Give the position of every leukocyte visible.
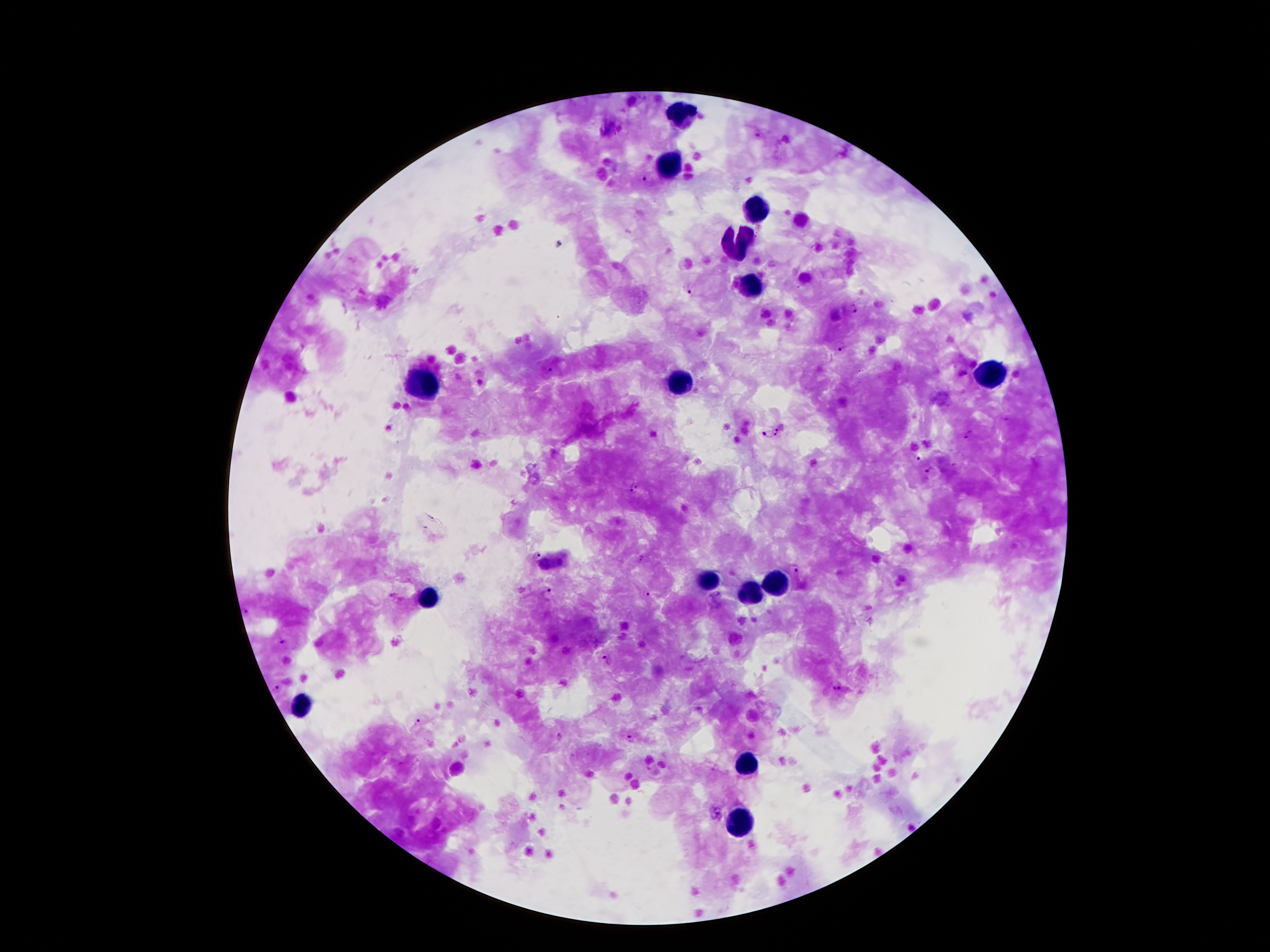

Approximate centers as [x, y] in pixels.
Leukocytes: [676, 115], [672, 163], [756, 207], [737, 241], [750, 287], [989, 375], [422, 383], [678, 385], [708, 581], [777, 581], [752, 593], [428, 598], [302, 707], [746, 763], [739, 822].

Malaria parasite locations: [758, 135], [644, 179], [690, 292], [853, 309], [842, 349], [551, 371], [779, 428], [768, 433], [969, 434], [777, 436], [919, 460], [931, 471], [634, 490], [536, 555], [794, 568], [548, 594], [647, 595], [248, 613], [283, 642], [608, 660], [278, 688], [838, 689], [418, 723], [559, 736], [631, 739]. One field from this slide. Patient malaria status: positive for Plasmodium falciparum. Photographed through the microscope eyepiece with a smartphone camera. Thick blood film. Image is 1270×952 pixels. Giemsa stain. 100x magnification.